Comment on the morphology of the red blood cells.
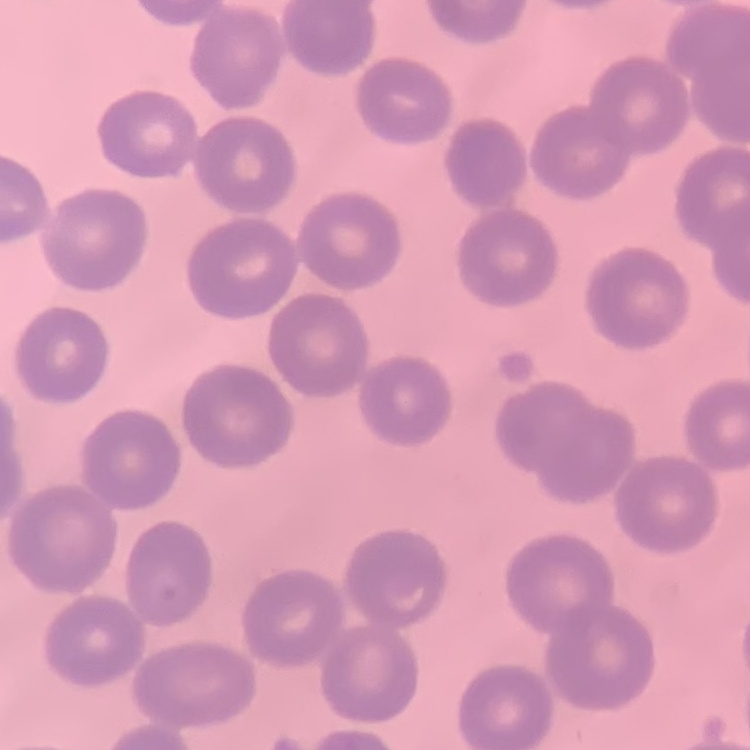
They show no rouleaux formation.

Summary:
  - Stain: Field's or Giemsa
  - Preparation: thin peripheral smear
  - Image type: one tile cut from a larger photomicrograph